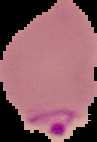

Summary:
  - Image type: segmented cell region with the area outside set to black
  - Preparation: thin blood film
  - Image size: 97×142 pixels
  - Malaria status: parasitized